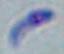

Summary:
  - Modality: micrograph
  - Magnification: 1000x
  - Identification: Toxoplasma gondii